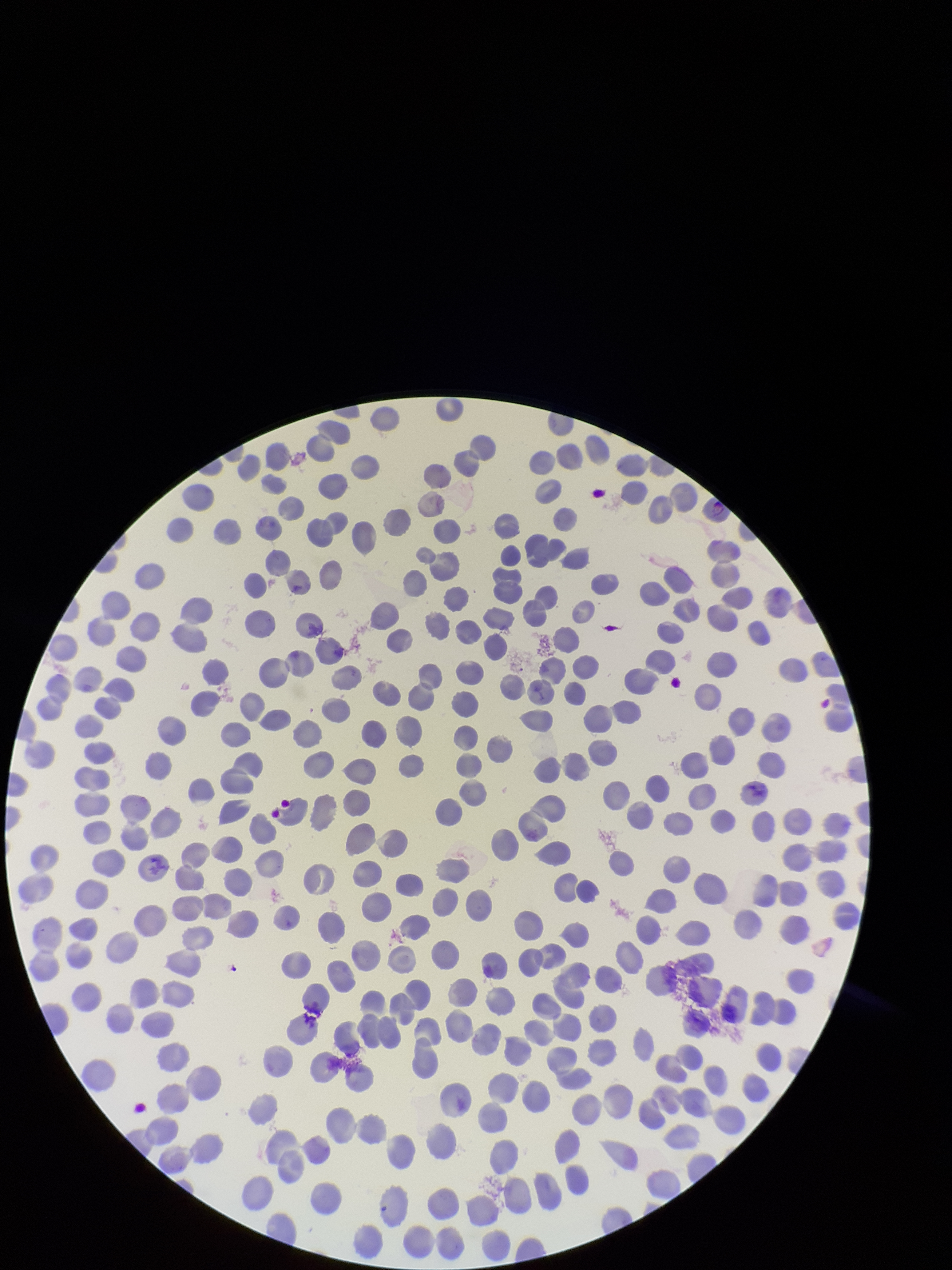
Species reported for this patient: Plasmodium vivax. Parasitized red blood cells: none seen. Giemsa stain. Smartphone photograph taken through the eyepiece of a microscope. Image is 952×1270 pixels. Patient malaria status: infected. Red blood cell count: 315. Single field of view. Preparation: thin smear. Parasitized red blood cell count: 0.